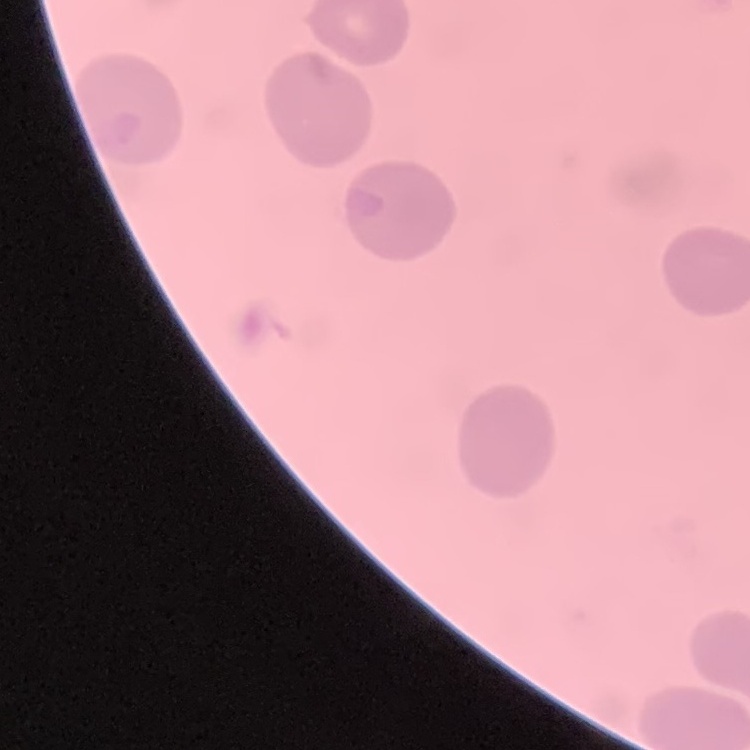
erythrocyte morphology = no rouleaux formation
preparation = thin peripheral smear
stain = Field's or Giemsa
image type = square crop of a larger photomicrograph